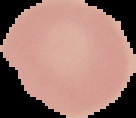
Summary:
  - Preparation: thin blood smear
  - Image type: cell region segmented out of the field of view; surrounding area masked to black
  - Malaria status: uninfected
  - Image size: 136×118 pixels